Name the parasite shown.
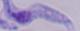
A trypanosome.

Summary:
  - Modality: micrograph
  - Magnification: 1000x